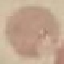

malaria status = uninfected
stain = Giemsa
capture = smartphone camera at the microscope eyepiece
preparation = thin blood film
image type = automatically extracted cell patch, resized to 64 × 64 pixels